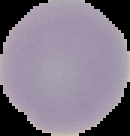

Summary:
  - Result: negative for Plasmodium parasites
  - Preparation: thin blood film
  - Image size: 130×136 pixels
  - Image type: segmented cell region with the area outside set to black